Assess this cell for malaria.
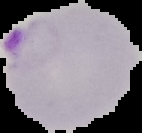

Parasitized.

Summary:
  - Image size: 142×133 pixels
  - Image type: segmented cell region with the area outside set to black
  - Preparation: thin blood smear